Identify the parasite.
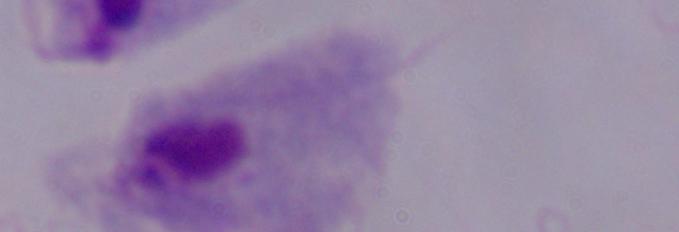
A trichomonad.

Summary:
  - Magnification: 1000x
  - Modality: photomicrograph